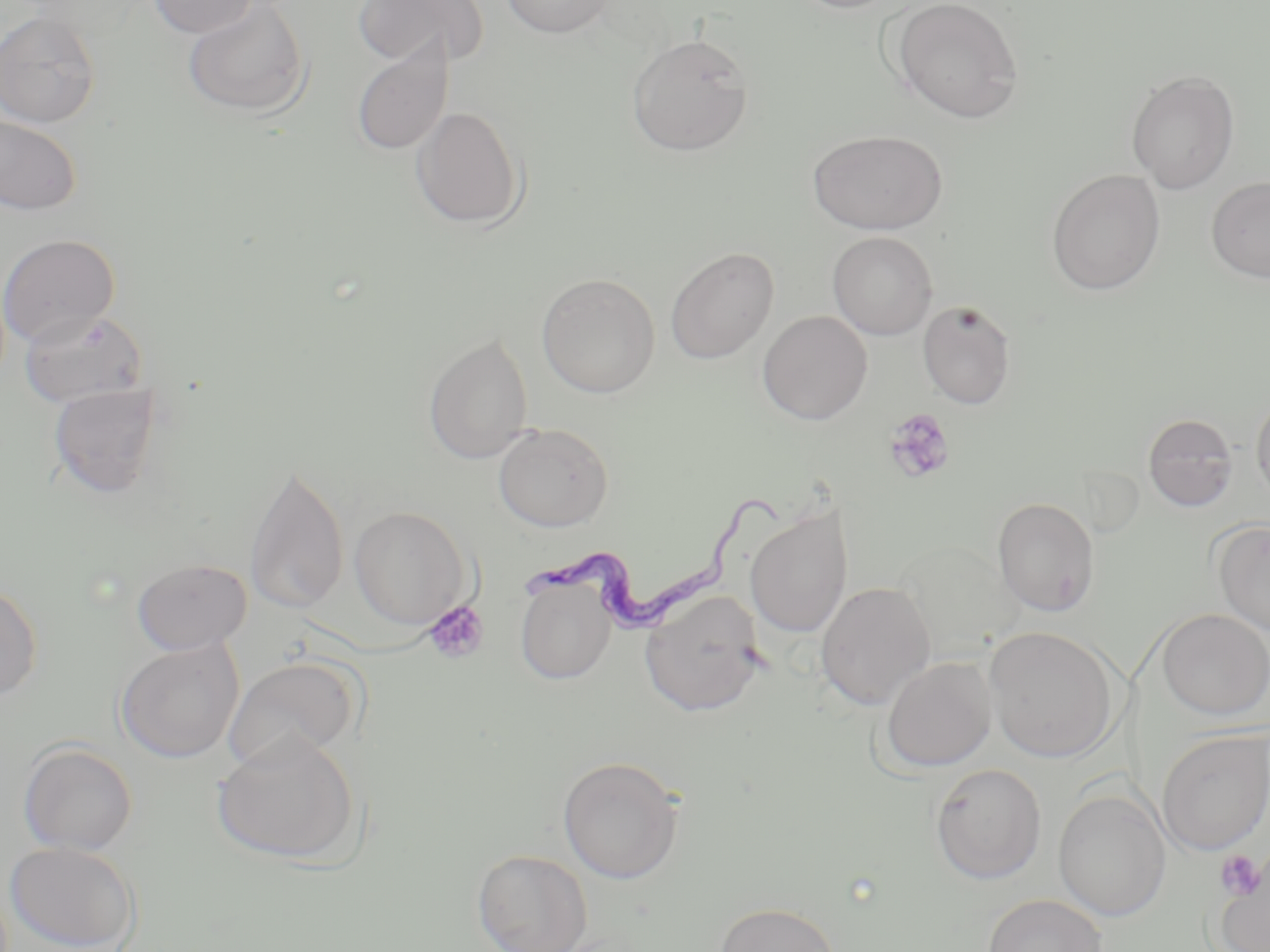
slide-level diagnosis = Trypanosoma brucei
preparation = thin blood film
Trypanosoma brucei locations = approximate bounding boxes as named x1/y1/x2/y2 corners in pixels: (x1=534, y1=494, x2=784, y2=628)
modality = light microscopy
image size = 1270×952 pixels
stain = May-Grünwald-Giemsa
platelet locations = approximate bounding boxes as named x1/y1/x2/y2 corners in pixels: (x1=882, y1=408, x2=956, y2=485), (x1=423, y1=600, x2=488, y2=664), (x1=1214, y1=849, x2=1267, y2=902)
field of view = one of a larger specimen
magnification = 1000x
uninfected red blood cell locations = approximate bounding boxes as named x1/y1/x2/y2 corners in pixels: (x1=148, y1=0, x2=259, y2=38), (x1=352, y1=0, x2=489, y2=68), (x1=500, y1=0, x2=615, y2=38), (x1=792, y1=0, x2=906, y2=14), (x1=891, y1=0, x2=1024, y2=123), (x1=183, y1=1, x2=311, y2=118), (x1=0, y1=9, x2=102, y2=129), (x1=626, y1=32, x2=754, y2=156), (x1=351, y1=38, x2=453, y2=156), (x1=1126, y1=69, x2=1240, y2=194), (x1=410, y1=105, x2=525, y2=230), (x1=0, y1=113, x2=83, y2=216), (x1=808, y1=129, x2=948, y2=235), (x1=1046, y1=169, x2=1166, y2=295), (x1=1206, y1=176, x2=1270, y2=283), (x1=828, y1=231, x2=937, y2=340), (x1=0, y1=233, x2=120, y2=347), (x1=665, y1=246, x2=780, y2=364), (x1=536, y1=273, x2=661, y2=398), (x1=917, y1=299, x2=1017, y2=409), (x1=19, y1=307, x2=149, y2=408), (x1=757, y1=310, x2=873, y2=424), (x1=423, y1=333, x2=534, y2=465), (x1=47, y1=382, x2=164, y2=499), (x1=1251, y1=390, x2=1270, y2=509), (x1=1143, y1=413, x2=1238, y2=512), (x1=492, y1=422, x2=614, y2=532), (x1=244, y1=460, x2=350, y2=615), (x1=992, y1=497, x2=1100, y2=617), (x1=744, y1=502, x2=854, y2=638), (x1=349, y1=506, x2=470, y2=629), (x1=1212, y1=519, x2=1270, y2=636), (x1=896, y1=541, x2=1024, y2=657), (x1=132, y1=558, x2=252, y2=655), (x1=514, y1=577, x2=617, y2=685), (x1=0, y1=580, x2=43, y2=703), (x1=815, y1=581, x2=935, y2=710), (x1=639, y1=589, x2=767, y2=716), (x1=1156, y1=609, x2=1270, y2=721), (x1=984, y1=626, x2=1120, y2=763), (x1=115, y1=638, x2=244, y2=763), (x1=881, y1=656, x2=997, y2=772), (x1=224, y1=657, x2=362, y2=771), (x1=1156, y1=728, x2=1270, y2=857), (x1=211, y1=731, x2=362, y2=867), (x1=18, y1=742, x2=138, y2=856), (x1=557, y1=756, x2=685, y2=883), (x1=929, y1=763, x2=1047, y2=884), (x1=1053, y1=788, x2=1172, y2=923), (x1=4, y1=840, x2=141, y2=951), (x1=472, y1=848, x2=593, y2=951), (x1=1216, y1=861, x2=1270, y2=952), (x1=982, y1=893, x2=1108, y2=952), (x1=714, y1=901, x2=840, y2=952)